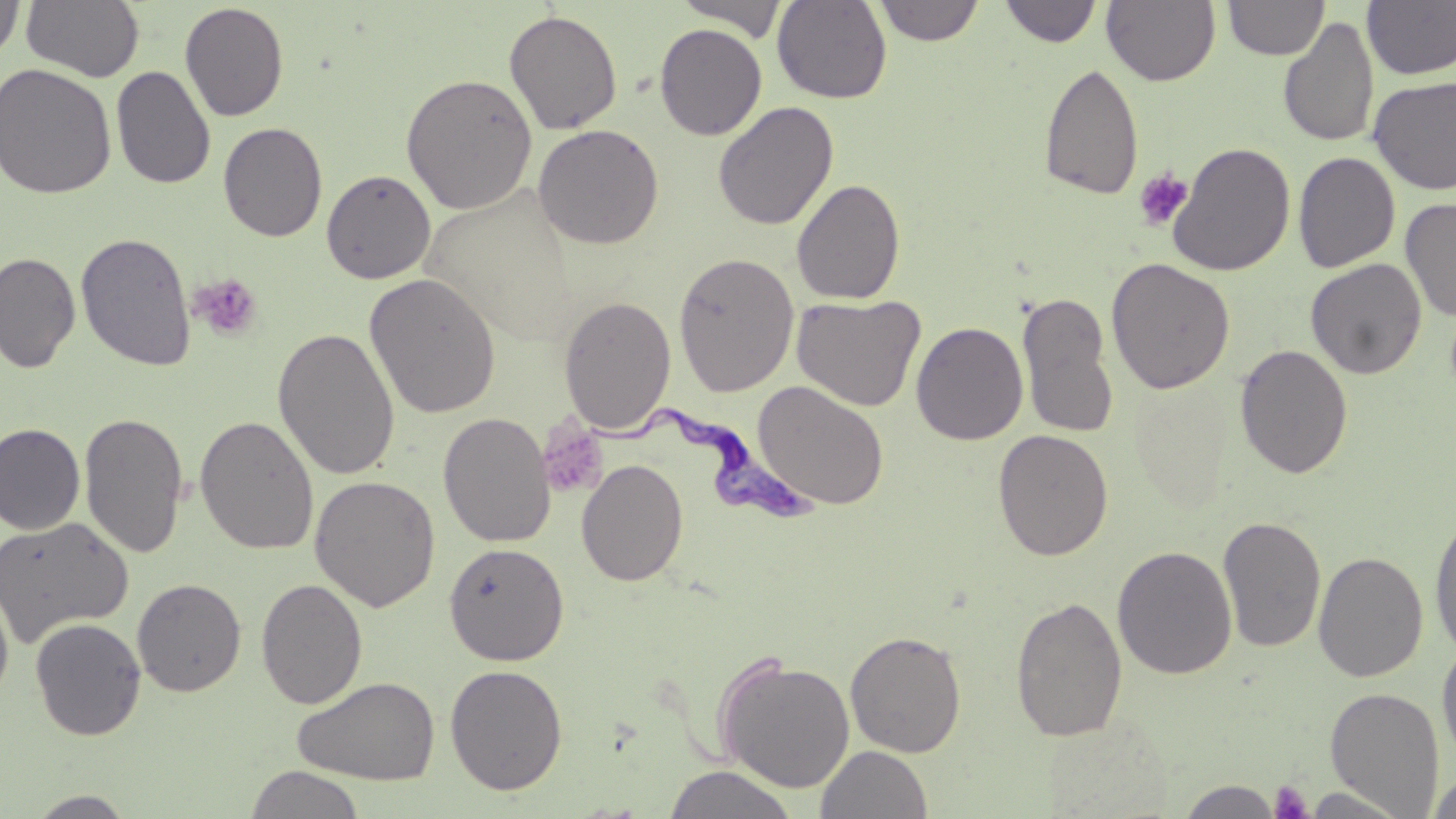 Approximate bounding boxes as (x1, y1, x2, y2) in pixels. Trypanosoma brucei locations: (587, 408, 822, 525). Platelet locations: (1133, 168, 1193, 231), (189, 273, 263, 341), (537, 421, 608, 499), (1269, 780, 1314, 819). Uninfected red blood cell locations: (0, 0, 26, 64), (21, 0, 144, 83), (675, 0, 788, 40), (772, 0, 892, 104), (874, 0, 984, 46), (1102, 0, 1220, 86), (999, 1, 1101, 47), (1223, 1, 1329, 60), (1362, 1, 1456, 80), (179, 2, 290, 122), (503, 9, 623, 135), (1279, 18, 1380, 148), (654, 23, 767, 140), (1039, 62, 1144, 201), (0, 63, 116, 199), (111, 65, 216, 190), (400, 72, 538, 215), (1367, 75, 1456, 196), (713, 101, 839, 230), (218, 123, 328, 242), (532, 124, 664, 249), (1167, 141, 1296, 277), (1292, 151, 1400, 273), (321, 169, 436, 284), (791, 178, 906, 305), (1400, 197, 1456, 322), (75, 232, 197, 372), (0, 251, 81, 373), (673, 251, 799, 397), (1105, 258, 1236, 394), (1305, 258, 1427, 379), (364, 272, 502, 419), (1016, 291, 1118, 440), (791, 293, 926, 412), (558, 295, 677, 433), (911, 321, 1029, 446), (272, 327, 400, 480), (1235, 343, 1354, 479), (753, 380, 889, 510), (79, 411, 190, 558), (438, 411, 555, 548), (194, 415, 319, 555), (0, 422, 85, 535), (992, 429, 1114, 561), (576, 458, 689, 587), (309, 475, 441, 611), (1428, 511, 1456, 660), (0, 516, 133, 647), (1218, 516, 1326, 653), (443, 541, 569, 665), (1112, 545, 1238, 679), (1313, 550, 1428, 683), (0, 578, 15, 706), (132, 578, 246, 697), (256, 578, 368, 709), (1010, 595, 1128, 742), (30, 617, 146, 740), (845, 629, 967, 758), (1436, 640, 1456, 768), (714, 654, 856, 794), (444, 663, 568, 795), (292, 675, 441, 786), (1325, 686, 1445, 816), (816, 745, 933, 818), (663, 764, 799, 819), (243, 765, 367, 819), (1428, 770, 1456, 819), (1176, 779, 1285, 818), (24, 791, 140, 818). Slide-level diagnosis: Trypanosoma brucei. One field of a larger specimen. Image is 1456×819 pixels. Light microscopy. Thin blood film. May-Grünwald-Giemsa stain. 1000x magnification.